Comment on the morphology of the red blood cells.
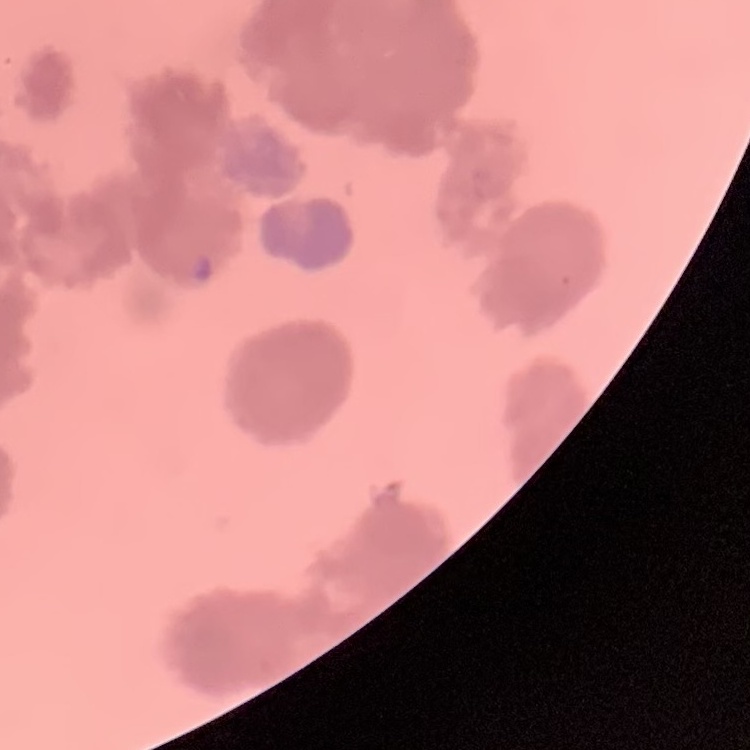

Rouleaux formation.

preparation: thin blood film
stain: Field's or Giemsa
image_type: one tile cut from a larger photomicrograph